Identify the parasite.
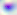

Toxoplasma gondii.

magnification = 400x
modality = photomicrograph